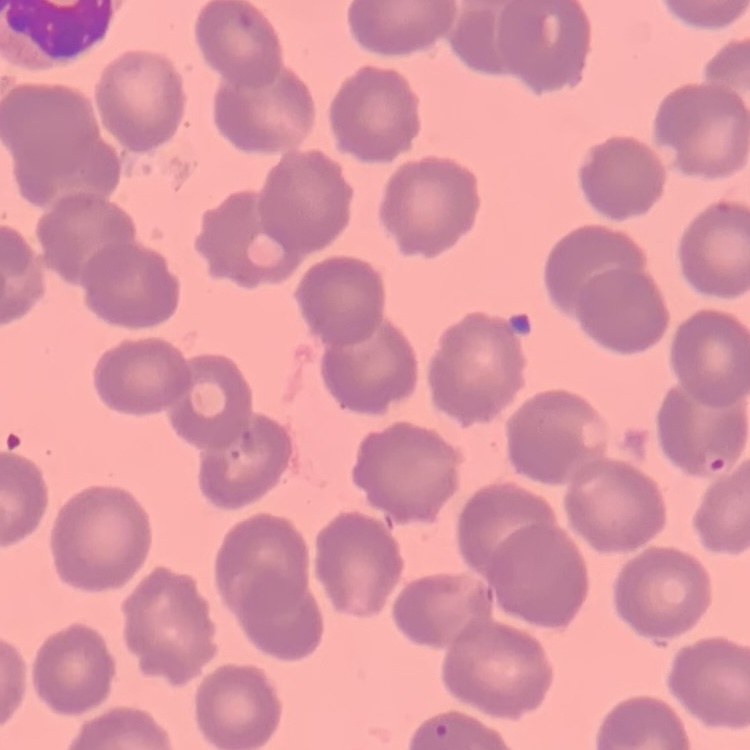

red_blood_cell_morphology: no rouleaux formation
image_type: one tile cut from a larger photomicrograph
preparation: thin blood film
stain: Field's or Giemsa